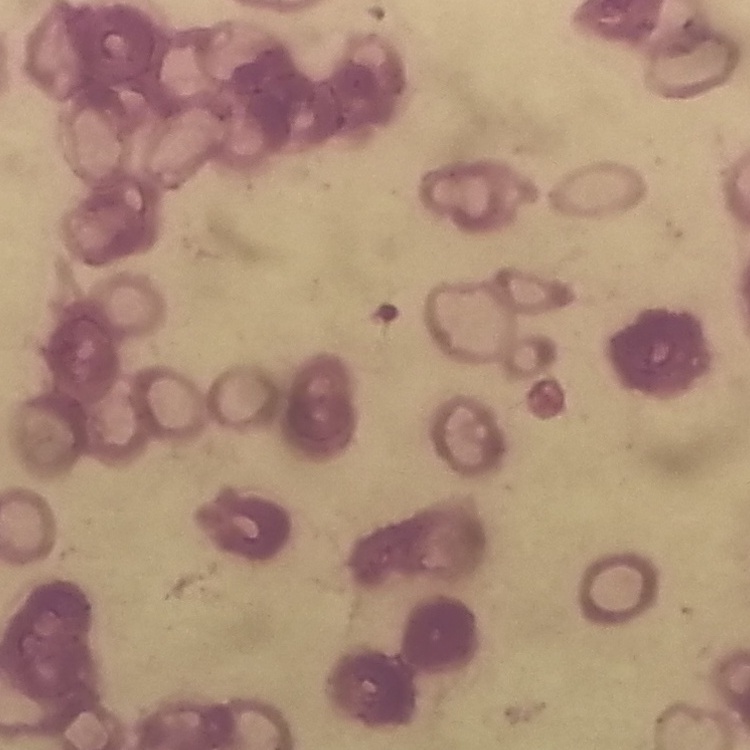 The erythrocytes show rouleaux formation. Stained with either Field's or Giemsa. Thin blood smear. Square crop of a larger photomicrograph.